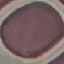

Summary:
  - Malaria status: uninfected
  - Stain: Giemsa
  - Preparation: thin blood film
  - Image type: automatically extracted cell patch, resized to 64 × 64 pixels
  - Capture: smartphone through the microscope eyepiece